Identify the preparation type.
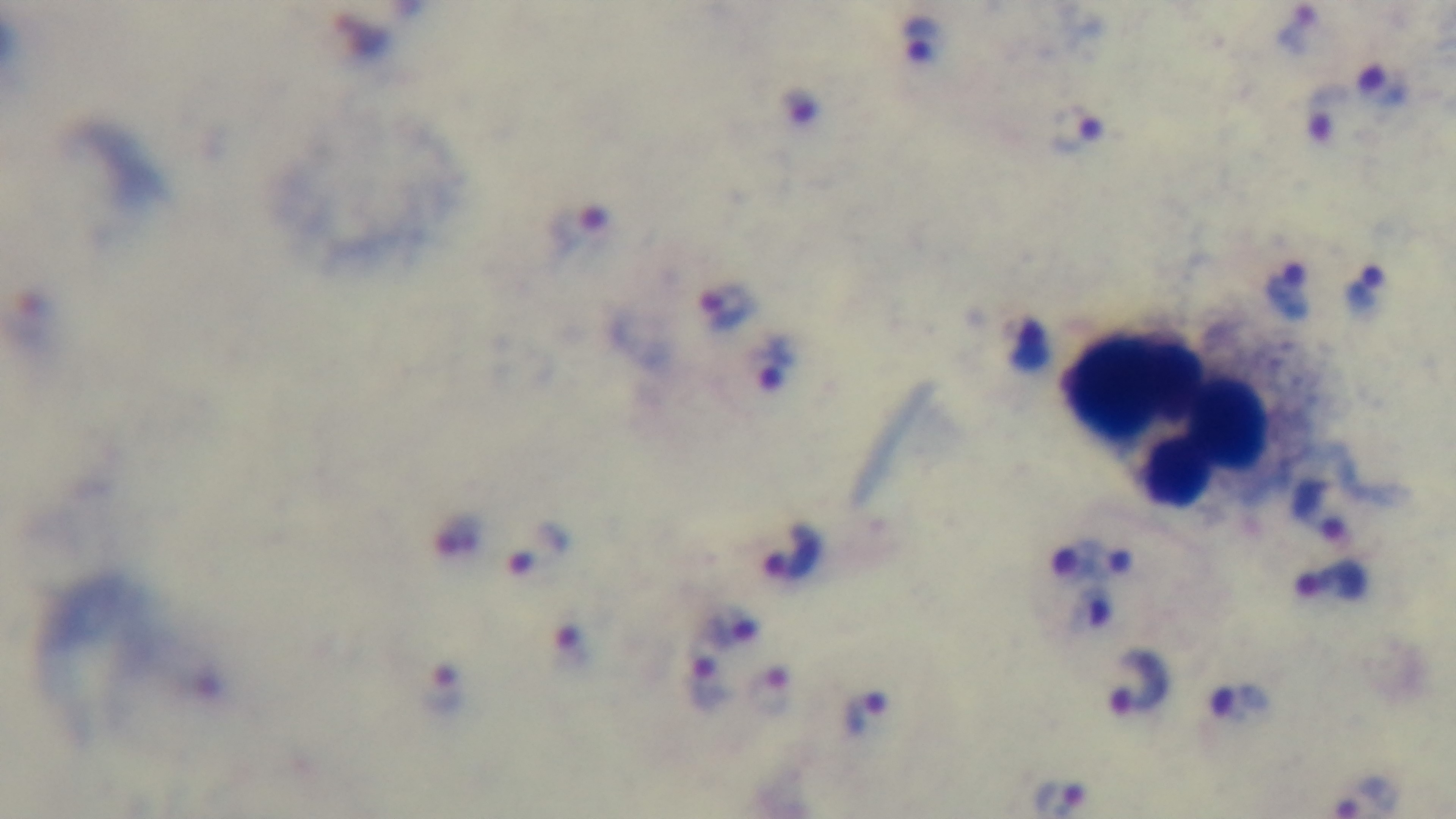
It is a thick blood film.

field of view = one from the slide
stain = Giemsa
capture = mounted 4K digital camera
modality = light microscopy
malaria status = infected
objective = 100x oil immersion